Locate every malaria parasite.
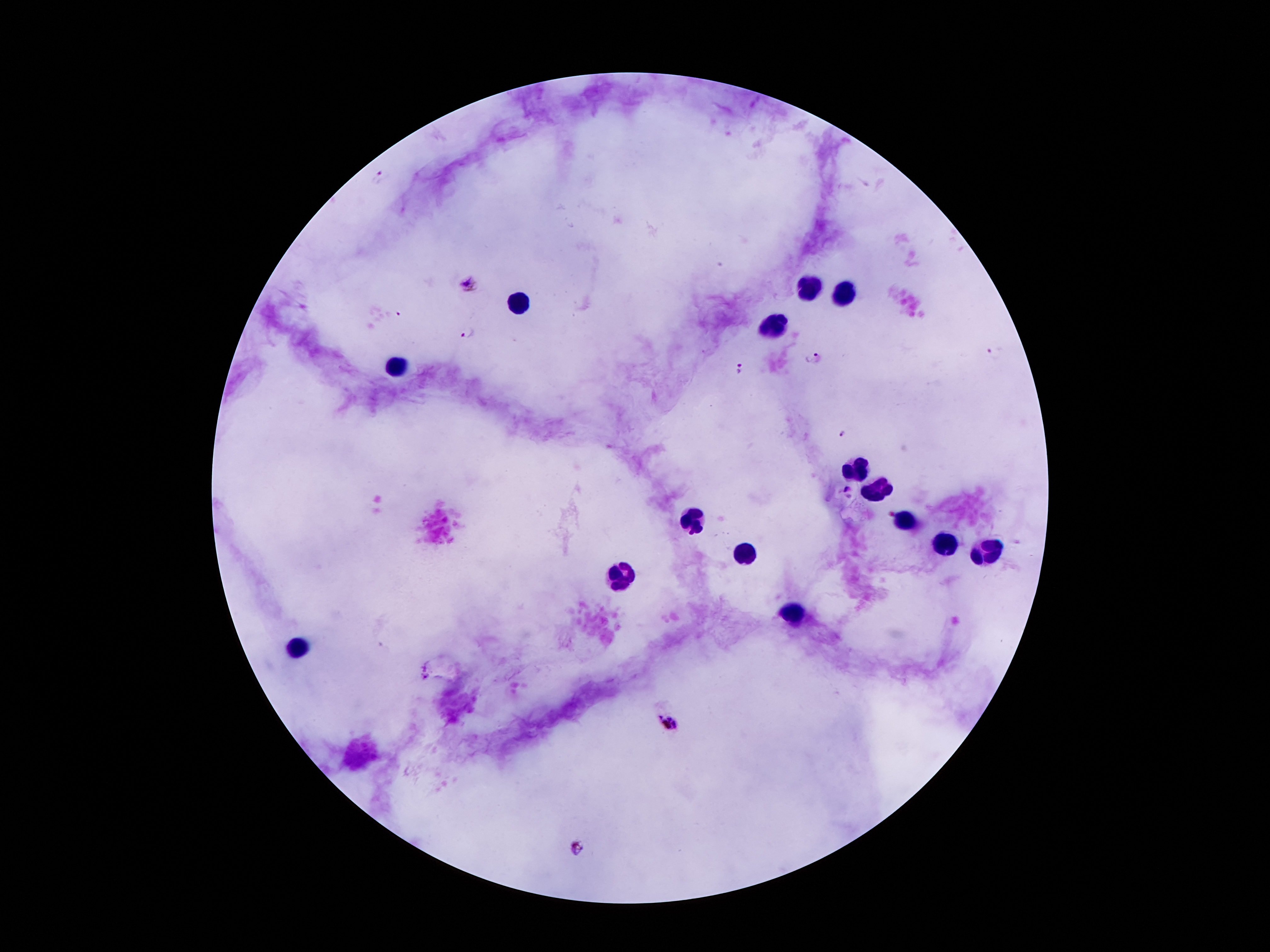
Approximate centers as (x, y) in pixels.
Malaria parasites: (378, 175), (469, 283), (398, 314), (466, 333), (993, 354), (816, 358), (738, 366), (843, 433), (846, 490), (889, 513), (424, 677), (668, 723), (575, 848).

image_size: 1270×952 pixels
capture: smartphone through the microscope eyepiece
preparation: thick blood smear
leukocyte_locations: 'approximate centers as (x, y) in pixels: (808, 287), (842, 291), (519, 303), (774, 325), (397, 364), (858, 471), (878, 489), (694, 518), (905, 521), (944, 545), (749, 552), (985, 552), (622, 575), (792, 616), (299, 645)'
field_of_view: one from this slide
magnification: 100x
stain: Giemsa
patient_malaria_status: positive for Plasmodium falciparum